Name the blood parasite species.
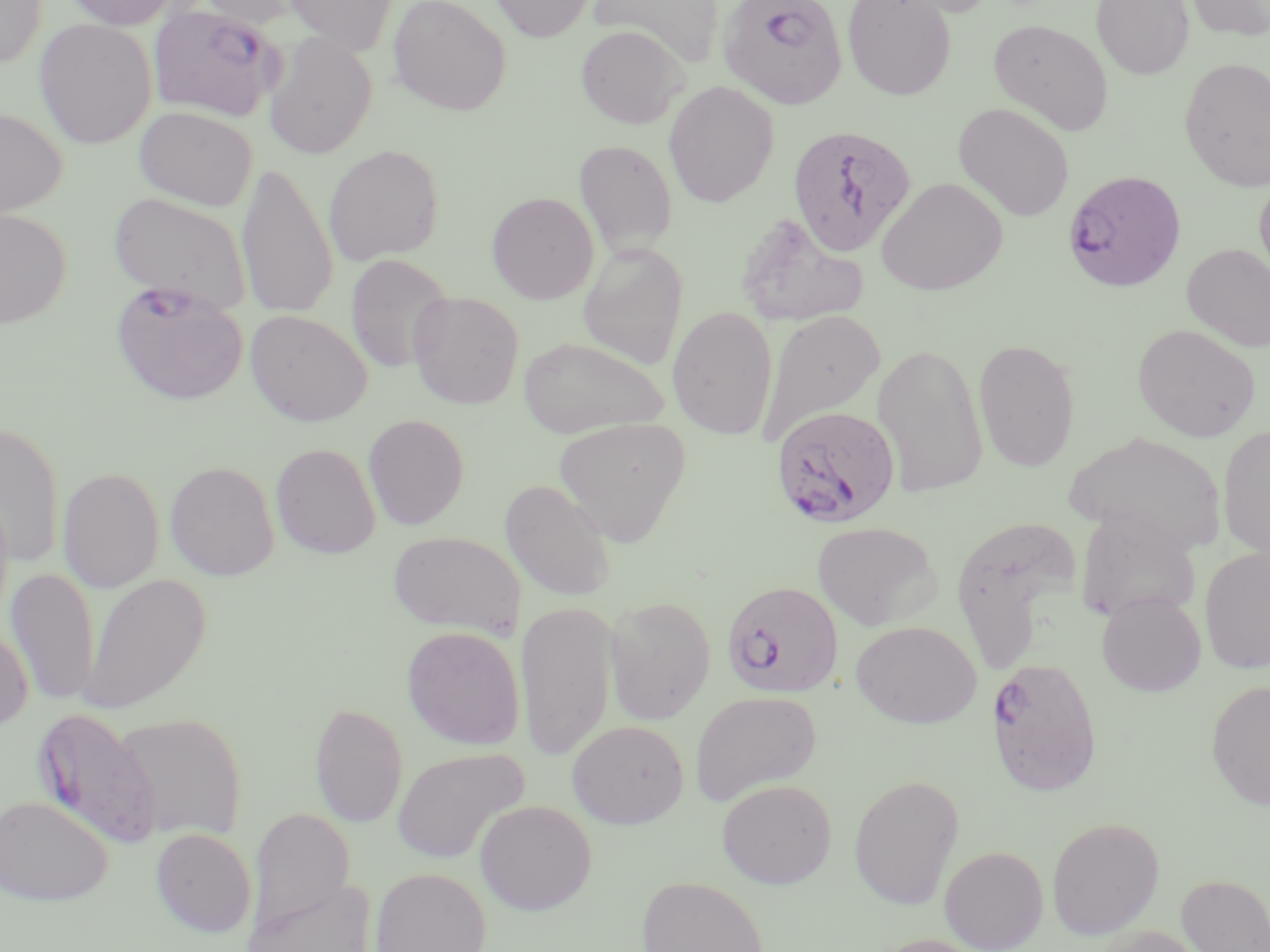

Plasmodium falciparum.

Summary:
  - Coordinate format: approximate bounding boxes as (x1, y1, x2, y2) in pixels
  - Plasmodium falciparum-infected red blood cell locations: (718, 0, 848, 110), (148, 3, 284, 122), (787, 124, 917, 256), (1062, 175, 1186, 299), (109, 281, 249, 406), (770, 405, 901, 529), (721, 580, 843, 699), (986, 655, 1102, 796), (33, 708, 161, 849)
  - Uninfected red blood cell locations: (0, 0, 47, 69), (62, 0, 183, 30), (194, 0, 306, 28), (283, 0, 398, 54), (388, 0, 512, 115), (488, 0, 595, 42), (588, 0, 724, 68), (842, 0, 956, 100), (887, 0, 1002, 18), (1091, 0, 1194, 80), (1184, 0, 1270, 42), (34, 18, 157, 149), (988, 18, 1114, 135), (576, 25, 687, 129), (263, 32, 377, 160), (1179, 57, 1270, 192), (663, 81, 779, 207), (953, 102, 1075, 222), (134, 105, 257, 210), (0, 107, 67, 219), (573, 139, 678, 258), (323, 144, 444, 265), (237, 161, 337, 320), (1254, 171, 1270, 289), (875, 177, 1008, 295), (108, 191, 253, 315), (487, 191, 599, 304), (0, 207, 72, 328), (735, 213, 871, 326), (577, 242, 688, 369), (1181, 243, 1270, 352), (346, 254, 453, 373), (407, 292, 525, 409), (667, 306, 778, 439), (244, 309, 373, 426), (758, 310, 885, 443), (1132, 323, 1261, 441), (517, 336, 668, 438), (973, 337, 1080, 473), (872, 341, 989, 499), (363, 414, 469, 530), (553, 416, 692, 545), (0, 421, 65, 569), (1217, 423, 1270, 561), (1067, 430, 1227, 555), (271, 442, 381, 559), (164, 460, 280, 581), (58, 466, 164, 592), (499, 478, 618, 602), (0, 489, 14, 626), (1076, 510, 1201, 624), (954, 517, 1085, 676), (811, 521, 942, 630), (388, 530, 525, 638), (1200, 546, 1270, 673), (5, 568, 100, 706), (79, 573, 211, 715), (1097, 590, 1206, 697), (603, 595, 716, 725), (516, 600, 618, 760), (850, 620, 982, 729), (0, 621, 33, 732), (401, 625, 525, 750), (1206, 679, 1270, 810), (690, 690, 822, 805), (309, 701, 408, 828), (112, 710, 247, 843), (568, 719, 689, 828), (391, 746, 529, 864), (849, 774, 964, 910), (716, 778, 837, 888), (0, 795, 113, 905), (474, 799, 597, 915), (248, 808, 355, 935), (1046, 816, 1165, 939), (150, 828, 256, 937), (939, 845, 1048, 951), (370, 867, 491, 952), (1177, 873, 1269, 952), (636, 875, 769, 952), (241, 878, 379, 952), (1092, 925, 1209, 952), (867, 934, 989, 952)
  - Field of view: one of a larger specimen
  - Stain: May-Grünwald-Giemsa
  - Image size: 1270×952 pixels
  - Magnification: 1000x
  - Preparation: thin blood smear
  - Modality: light microscopy